Assess the morphology of the erythrocytes.
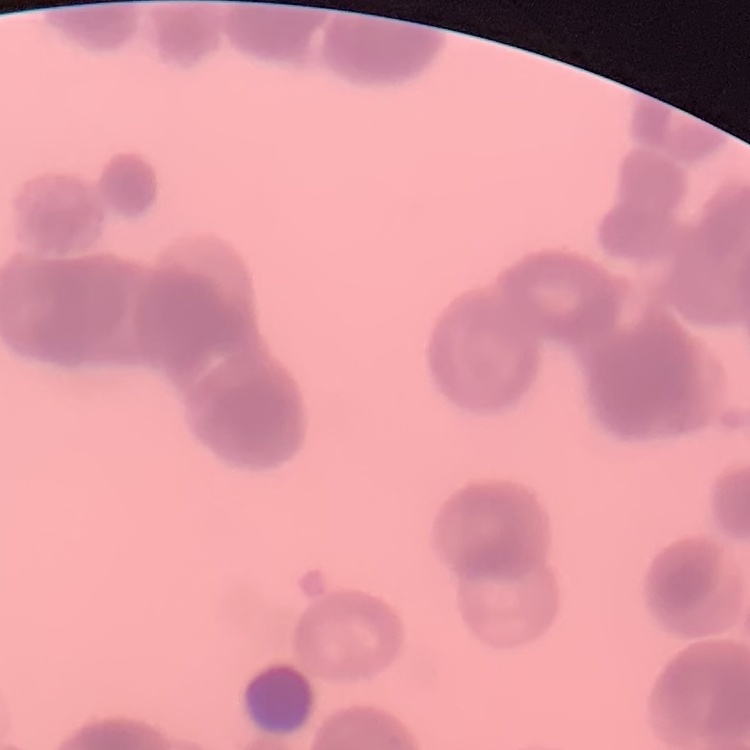

Rouleaux formation.

{
  "preparation": "thin blood smear",
  "stain": "Field's or Giemsa",
  "image_type": "one tile cut from a larger photomicrograph"
}